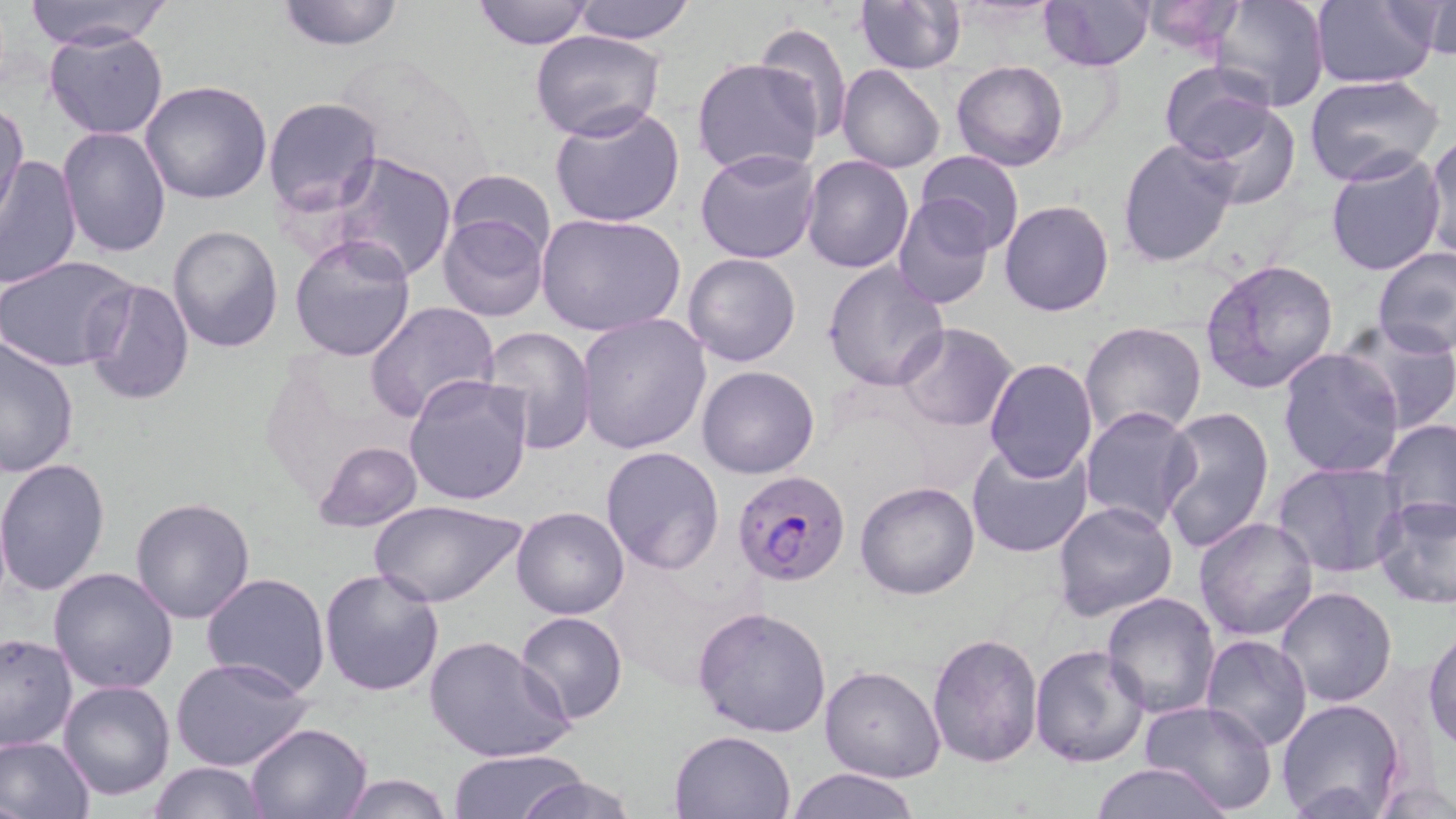

Approximate bounding boxes as (x1, y1, x2, y2) in pixels. Plasmodium falciparum-infected red blood cell locations: (732, 470, 852, 586). Uninfected red blood cell locations: (273, 0, 407, 51), (470, 0, 594, 49), (572, 0, 697, 43), (854, 0, 966, 74), (1040, 0, 1154, 71), (1136, 0, 1250, 58), (1310, 0, 1438, 88), (25, 1, 172, 50), (1207, 1, 1330, 112), (1411, 1, 1454, 59), (755, 21, 853, 144), (44, 27, 169, 139), (532, 31, 664, 142), (692, 58, 823, 179), (952, 59, 1068, 171), (1137, 60, 1270, 259), (1158, 62, 1282, 169), (837, 64, 945, 173), (1304, 73, 1443, 185), (139, 80, 273, 205), (263, 97, 383, 218), (0, 99, 28, 222), (1187, 102, 1303, 207), (549, 103, 686, 228), (57, 127, 172, 259), (1423, 133, 1456, 260), (1116, 136, 1239, 267), (695, 148, 822, 263), (915, 149, 1026, 254), (1324, 150, 1448, 276), (0, 152, 83, 293), (329, 152, 458, 282), (802, 154, 916, 273), (447, 169, 556, 260), (891, 194, 994, 310), (1000, 200, 1115, 317), (436, 211, 548, 321), (536, 212, 686, 337), (168, 225, 284, 353), (290, 234, 417, 362), (1374, 247, 1456, 360), (683, 253, 800, 367), (0, 255, 137, 372), (1199, 258, 1341, 397), (821, 260, 949, 392), (83, 279, 195, 406), (365, 302, 499, 425), (577, 312, 712, 454), (1079, 321, 1206, 441), (1338, 321, 1456, 433), (893, 322, 1019, 433), (482, 327, 599, 455), (0, 331, 79, 476), (1276, 347, 1405, 481), (984, 358, 1098, 482), (697, 365, 820, 479), (401, 372, 533, 506), (1079, 406, 1200, 533), (1158, 407, 1275, 552), (1378, 417, 1456, 531), (965, 439, 1095, 558), (312, 440, 423, 533), (599, 445, 725, 575), (0, 457, 114, 597), (1270, 462, 1407, 579), (855, 481, 980, 600), (1372, 493, 1456, 609), (369, 496, 525, 608), (130, 497, 256, 624), (1051, 500, 1181, 624), (512, 506, 629, 619), (1194, 517, 1320, 640), (47, 567, 179, 695), (318, 568, 447, 697), (200, 572, 331, 698), (1275, 586, 1399, 708), (1099, 591, 1220, 719), (692, 604, 834, 740), (516, 612, 628, 726), (1425, 628, 1456, 749), (0, 632, 76, 751), (926, 632, 1043, 768), (424, 634, 575, 764), (1200, 636, 1314, 753), (1028, 644, 1150, 769), (170, 655, 315, 772), (819, 665, 946, 783), (59, 681, 176, 802), (1276, 698, 1406, 819), (1140, 700, 1281, 817), (244, 722, 372, 817), (671, 730, 798, 818), (0, 734, 95, 819), (447, 749, 585, 818), (146, 760, 272, 818), (1086, 761, 1235, 818), (786, 767, 920, 819), (518, 771, 637, 819), (336, 772, 454, 818). Slide-level diagnosis: Plasmodium falciparum. One field of a larger specimen. Thin blood smear. May-Grünwald-Giemsa-stained preparation. Image is 1456×819 pixels. 1000x magnification. Light microscopy.